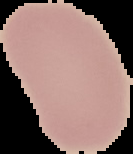

Summary:
  - Preparation: thin blood smear
  - Image size: 133×154 pixels
  - Image type: segmented cell region on a black background
  - Result: negative for Plasmodium parasites